Classify the preparation.
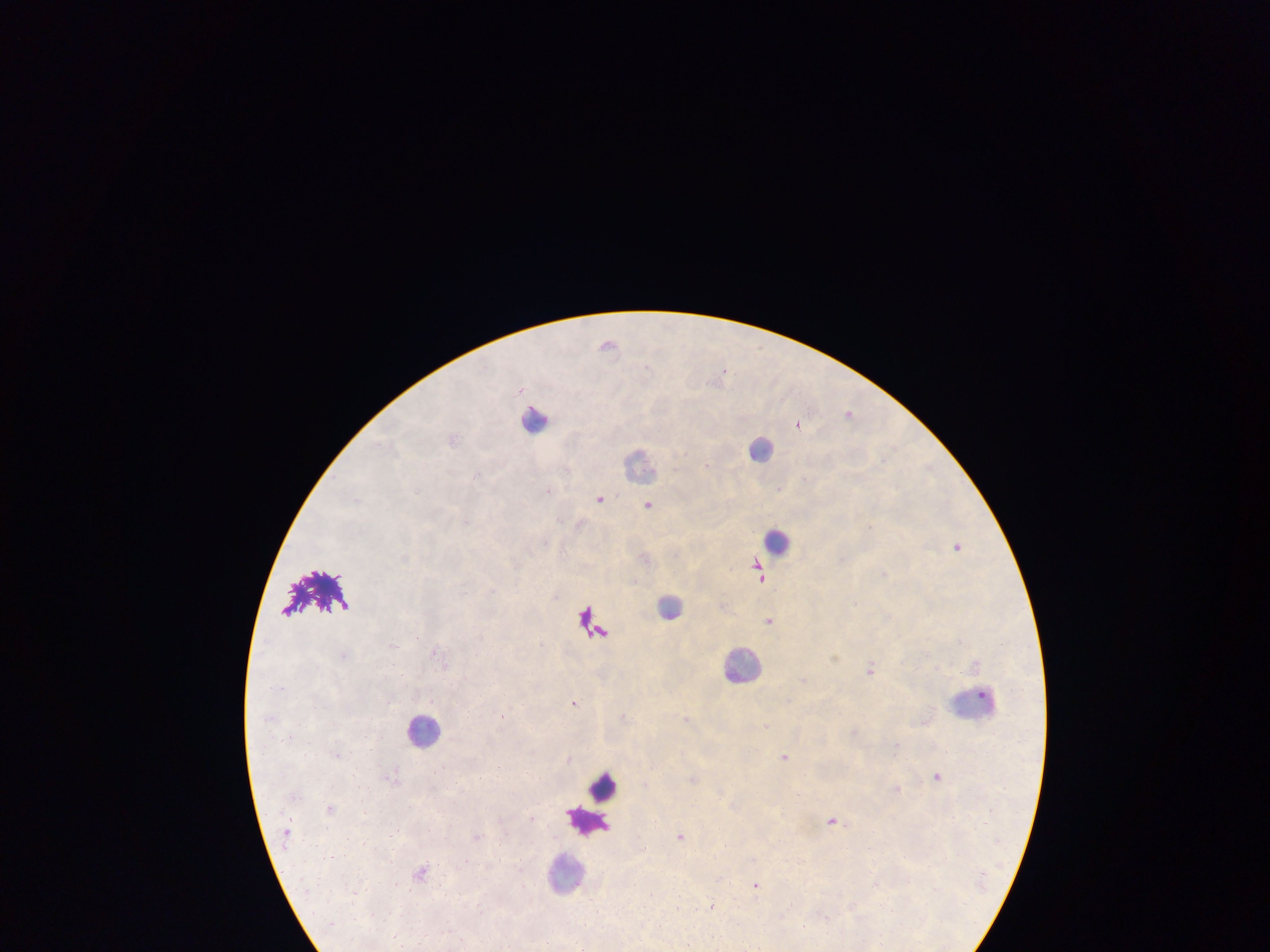

Thick blood smear.

Approximate centers as x y in pixels. Plasmodium parasite locations: 608 344; 725 370; 848 412; 798 424; 453 440; 708 465; 477 474; 547 491; 601 497; 356 500; 649 504; 466 521; 770 620; 344 654; 871 669; 573 702; 502 716; 785 756; 569 757; 938 776; 833 820; 681 835; 477 836; 725 845; 756 886; 712 906. Leukocyte locations: 535 420; 762 448; 640 465; 777 541; 670 605; 742 664; 974 702; 424 729; 604 787; 586 821; 565 872. Single field of view. Image is 1270×952 pixels. Photographed through a microscope with a mobile-phone camera. Collected in Ghana.